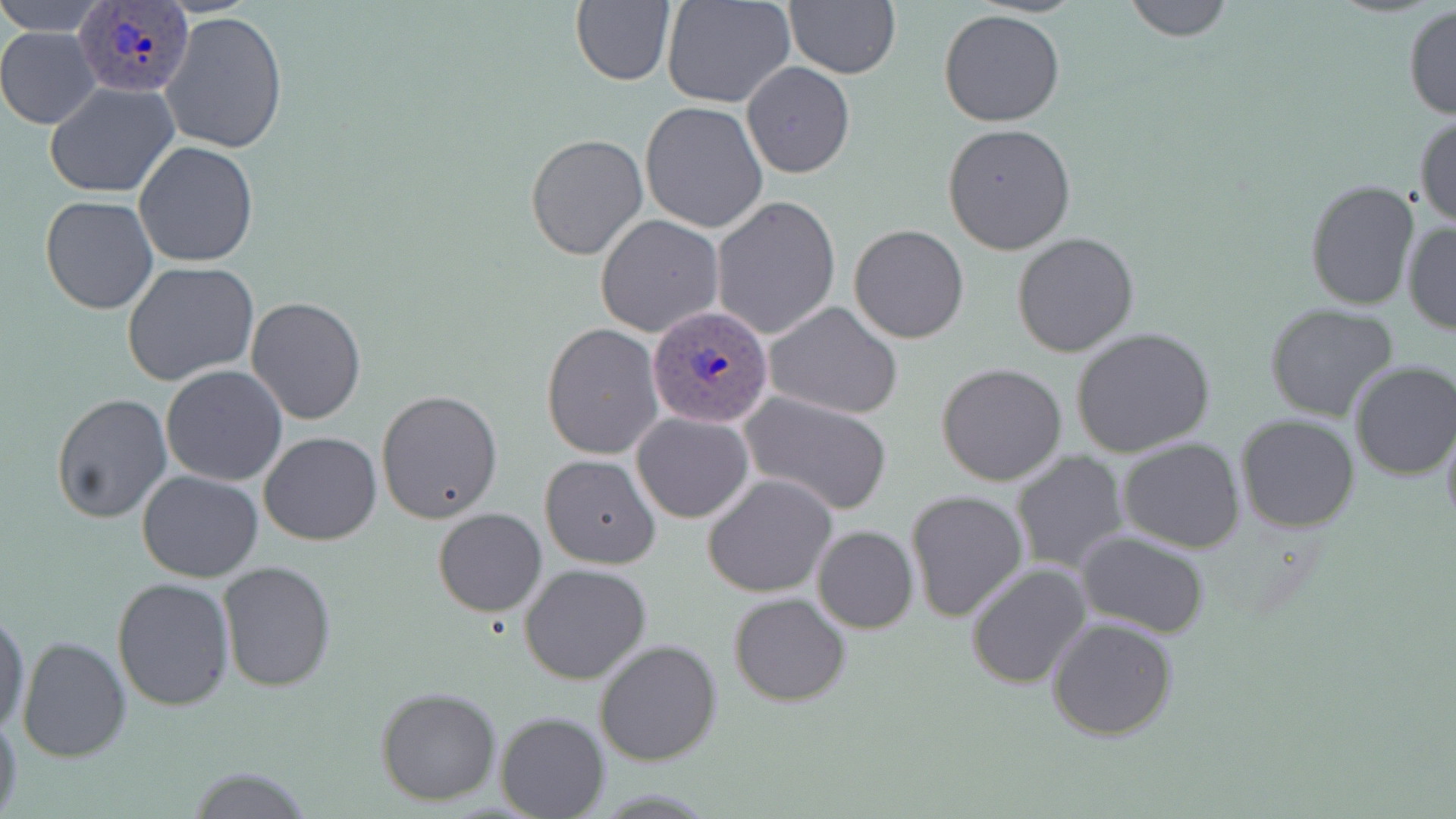
Approximate bounding boxes as named x1/y1/x2/y2 corners in pixels. Plasmodium ovale-infected red blood cell locations: (x1=74, y1=5, x2=190, y2=95), (x1=646, y1=304, x2=774, y2=428). Uninfected red blood cell locations: (x1=2, y1=0, x2=108, y2=32), (x1=570, y1=0, x2=678, y2=87), (x1=662, y1=0, x2=797, y2=109), (x1=1120, y1=0, x2=1235, y2=43), (x1=784, y1=1, x2=901, y2=79), (x1=1402, y1=4, x2=1456, y2=120), (x1=939, y1=9, x2=1067, y2=127), (x1=159, y1=11, x2=289, y2=156), (x1=0, y1=28, x2=99, y2=129), (x1=742, y1=62, x2=855, y2=179), (x1=45, y1=82, x2=179, y2=198), (x1=639, y1=101, x2=768, y2=233), (x1=1413, y1=111, x2=1456, y2=229), (x1=942, y1=122, x2=1076, y2=254), (x1=525, y1=133, x2=649, y2=261), (x1=135, y1=141, x2=258, y2=267), (x1=1304, y1=179, x2=1421, y2=310), (x1=40, y1=195, x2=159, y2=315), (x1=710, y1=197, x2=841, y2=340), (x1=595, y1=214, x2=725, y2=338), (x1=1402, y1=220, x2=1455, y2=335), (x1=849, y1=224, x2=969, y2=344), (x1=1012, y1=231, x2=1141, y2=358), (x1=122, y1=262, x2=261, y2=387), (x1=246, y1=297, x2=366, y2=426), (x1=762, y1=301, x2=904, y2=419), (x1=1264, y1=302, x2=1401, y2=423), (x1=541, y1=324, x2=664, y2=460), (x1=1069, y1=326, x2=1215, y2=457), (x1=1347, y1=360, x2=1456, y2=481), (x1=936, y1=362, x2=1067, y2=486), (x1=161, y1=365, x2=288, y2=485), (x1=376, y1=389, x2=504, y2=523), (x1=51, y1=391, x2=172, y2=524), (x1=739, y1=391, x2=893, y2=515), (x1=724, y1=402, x2=882, y2=613), (x1=632, y1=412, x2=754, y2=523), (x1=1234, y1=414, x2=1361, y2=533), (x1=1441, y1=419, x2=1456, y2=537), (x1=259, y1=430, x2=382, y2=545), (x1=1118, y1=437, x2=1245, y2=553), (x1=1009, y1=450, x2=1130, y2=575), (x1=540, y1=453, x2=661, y2=568), (x1=137, y1=470, x2=264, y2=582), (x1=703, y1=474, x2=837, y2=596), (x1=905, y1=489, x2=1029, y2=621), (x1=432, y1=507, x2=547, y2=617), (x1=811, y1=525, x2=919, y2=633), (x1=1075, y1=530, x2=1211, y2=639), (x1=217, y1=560, x2=337, y2=692), (x1=519, y1=562, x2=652, y2=686), (x1=967, y1=562, x2=1094, y2=689), (x1=112, y1=577, x2=235, y2=710), (x1=729, y1=592, x2=852, y2=707), (x1=0, y1=606, x2=30, y2=737), (x1=1046, y1=616, x2=1179, y2=741), (x1=16, y1=634, x2=131, y2=762), (x1=594, y1=639, x2=722, y2=767), (x1=375, y1=686, x2=501, y2=806), (x1=0, y1=707, x2=23, y2=819), (x1=495, y1=711, x2=609, y2=817), (x1=178, y1=767, x2=315, y2=819). Slide-level diagnosis: Plasmodium ovale. One field of a larger specimen. Image is 1456×819 pixels. Thin blood film. Optical microscopy. May-Grünwald-Giemsa stain. Captured at 1000x magnification.